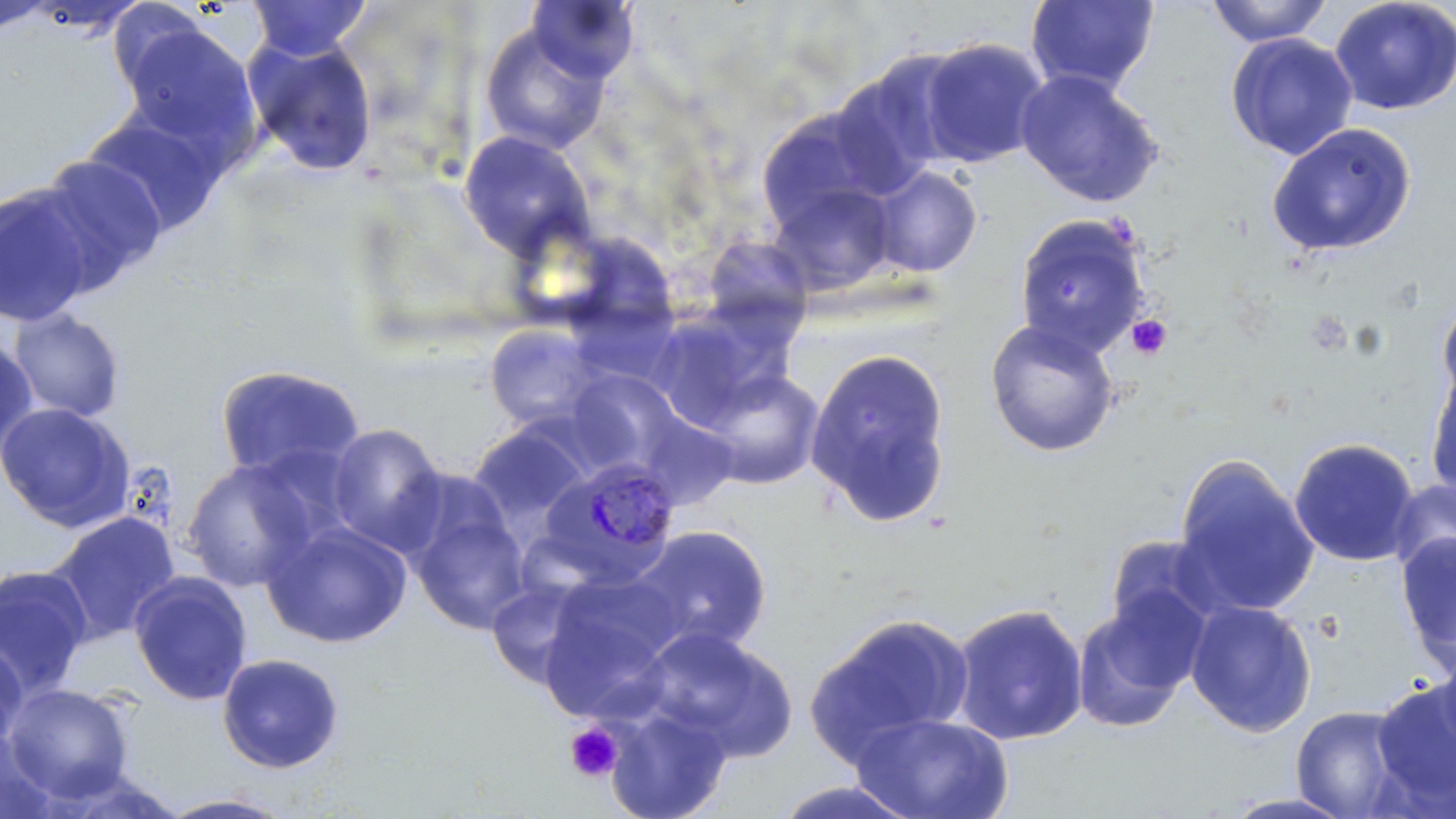

Summary:
  - Coordinate format: approximate bounding boxes as named x1/y1/x2/y2 corners in pixels
  - Platelet locations: (x1=1304, y1=309, x2=1353, y2=356), (x1=1126, y1=314, x2=1173, y2=361), (x1=563, y1=722, x2=625, y2=783)
  - Plasmodium malariae-infected red blood cell locations: (x1=538, y1=457, x2=682, y2=588)
  - Uninfected red blood cell locations: (x1=247, y1=0, x2=372, y2=60), (x1=526, y1=0, x2=640, y2=83), (x1=1025, y1=0, x2=1160, y2=96), (x1=1204, y1=0, x2=1334, y2=47), (x1=1329, y1=0, x2=1456, y2=116), (x1=0, y1=2, x2=54, y2=36), (x1=118, y1=21, x2=262, y2=159), (x1=478, y1=23, x2=613, y2=156), (x1=1225, y1=33, x2=1358, y2=160), (x1=242, y1=34, x2=380, y2=177), (x1=915, y1=37, x2=1051, y2=168), (x1=828, y1=50, x2=970, y2=194), (x1=1014, y1=69, x2=1165, y2=209), (x1=754, y1=107, x2=890, y2=235), (x1=80, y1=109, x2=228, y2=240), (x1=1266, y1=122, x2=1417, y2=257), (x1=458, y1=130, x2=594, y2=259), (x1=34, y1=155, x2=167, y2=290), (x1=866, y1=165, x2=982, y2=277), (x1=767, y1=180, x2=899, y2=297), (x1=1, y1=182, x2=100, y2=329), (x1=1013, y1=213, x2=1151, y2=357), (x1=561, y1=229, x2=680, y2=343), (x1=700, y1=234, x2=814, y2=337), (x1=1436, y1=289, x2=1456, y2=412), (x1=649, y1=304, x2=797, y2=426), (x1=7, y1=308, x2=128, y2=422), (x1=984, y1=317, x2=1121, y2=458), (x1=484, y1=324, x2=605, y2=433), (x1=0, y1=336, x2=38, y2=462), (x1=804, y1=348, x2=953, y2=528), (x1=1425, y1=363, x2=1456, y2=503), (x1=213, y1=364, x2=366, y2=484), (x1=696, y1=367, x2=826, y2=490), (x1=562, y1=368, x2=685, y2=477), (x1=0, y1=402, x2=135, y2=531), (x1=467, y1=422, x2=594, y2=543), (x1=325, y1=423, x2=447, y2=554), (x1=1289, y1=437, x2=1420, y2=567), (x1=1173, y1=455, x2=1319, y2=619), (x1=181, y1=457, x2=318, y2=593), (x1=1388, y1=476, x2=1456, y2=582), (x1=406, y1=500, x2=531, y2=634), (x1=44, y1=511, x2=181, y2=645), (x1=261, y1=519, x2=413, y2=649), (x1=628, y1=524, x2=773, y2=654), (x1=1395, y1=531, x2=1456, y2=669), (x1=1105, y1=534, x2=1223, y2=638), (x1=0, y1=565, x2=94, y2=700), (x1=128, y1=570, x2=254, y2=706), (x1=538, y1=573, x2=682, y2=716), (x1=485, y1=577, x2=601, y2=687), (x1=1069, y1=595, x2=1203, y2=734), (x1=1185, y1=600, x2=1318, y2=737), (x1=950, y1=602, x2=1089, y2=746), (x1=806, y1=613, x2=974, y2=762), (x1=636, y1=625, x2=798, y2=761), (x1=0, y1=642, x2=27, y2=753), (x1=1429, y1=643, x2=1456, y2=766), (x1=216, y1=652, x2=345, y2=774), (x1=1369, y1=678, x2=1456, y2=811), (x1=4, y1=682, x2=134, y2=802), (x1=605, y1=702, x2=734, y2=819), (x1=1289, y1=704, x2=1415, y2=818), (x1=850, y1=712, x2=1015, y2=819), (x1=0, y1=728, x2=63, y2=819), (x1=765, y1=780, x2=926, y2=819), (x1=1218, y1=791, x2=1357, y2=818), (x1=154, y1=792, x2=299, y2=818)
  - Slide-level diagnosis: Plasmodium malariae
  - Image size: 1456×819 pixels
  - Modality: light microscopy
  - Preparation: thin blood film
  - Stain: May-Grünwald-Giemsa
  - Magnification: 1000x
  - Field of view: one of a larger specimen